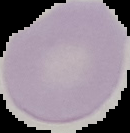

Summary:
  - Preparation: thin blood smear
  - Image type: segmented cell region on a black background
  - Image size: 130×133 pixels
  - Malaria status: uninfected